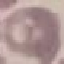
Summary:
  - Malaria status: uninfected
  - Preparation: thin blood smear
  - Image type: cell patch, automatically extracted from a larger field of view and resized to 64 × 64 pixels
  - Stain: Giemsa
  - Capture: smartphone through the microscope eyepiece